Give the extent of all Babesia divergens-infected red blood cells.
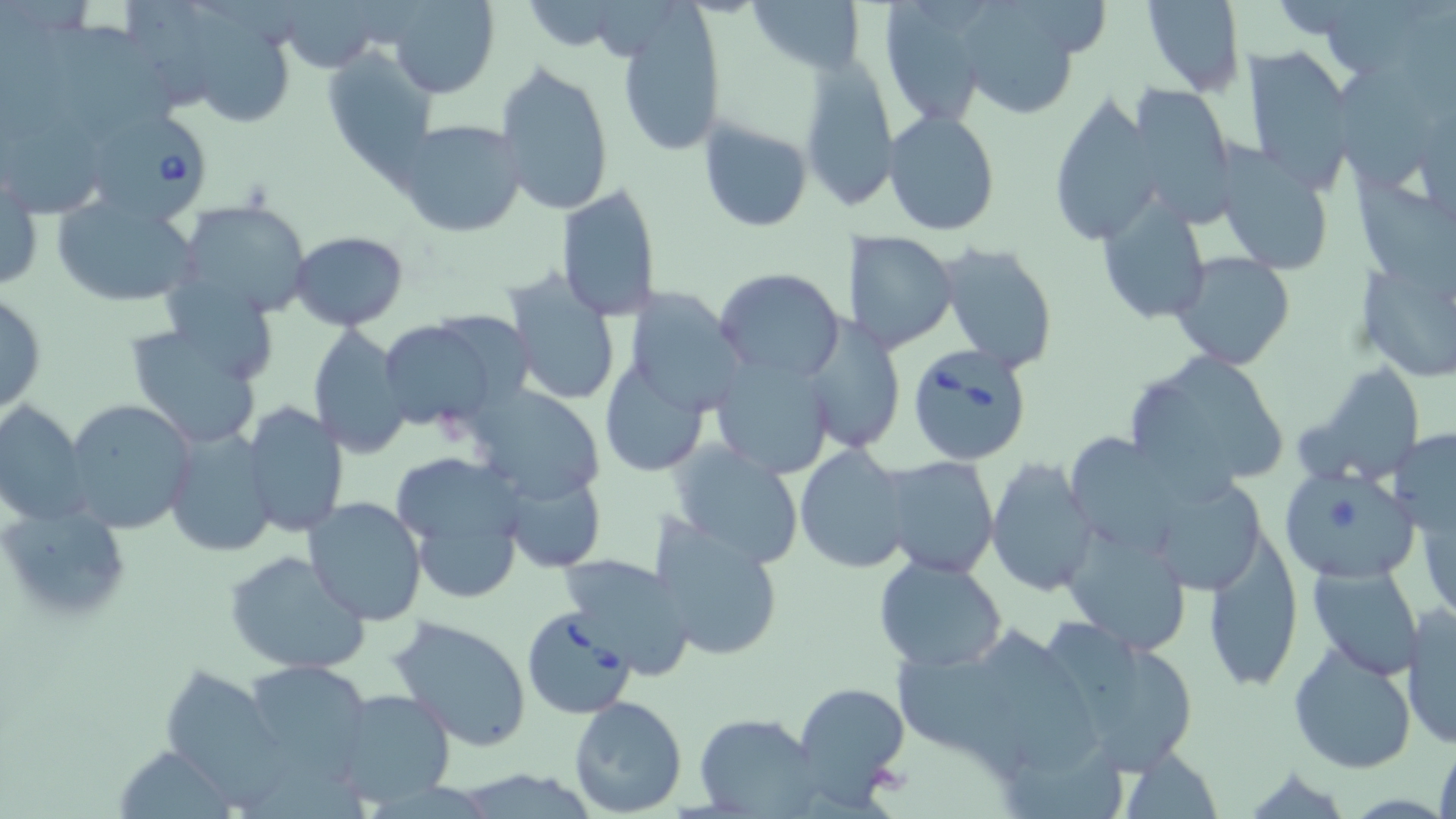
Approximate bounding boxes as (x1,y1)-(x2,y2) corner pairs in pixels.
Babesia divergens-infected red blood cells: (90,111)-(217,227), (905,342)-(1034,465), (521,607)-(637,721).

Uninfected red blood cell locations: (280,0)-(385,73), (387,0)-(500,99), (872,0)-(993,128), (1142,0)-(1244,95), (182,1)-(293,123), (747,1)-(867,74), (951,1)-(1092,122), (615,9)-(726,160), (47,18)-(178,137), (1238,45)-(1354,191), (322,49)-(438,175), (798,56)-(898,207), (495,59)-(616,218), (1336,65)-(1434,194), (1127,82)-(1238,223), (1046,93)-(1166,246), (882,110)-(1001,237), (396,118)-(527,237), (698,118)-(814,231), (0,119)-(114,217), (1214,147)-(1336,276), (1357,166)-(1456,292), (1,170)-(43,295), (554,182)-(661,321), (51,192)-(202,308), (176,197)-(312,317), (1098,200)-(1211,326), (848,230)-(959,353), (288,231)-(408,331), (935,242)-(1060,373), (1169,252)-(1296,371), (1358,259)-(1455,385), (503,267)-(626,408), (715,268)-(845,382), (620,289)-(746,418), (0,291)-(47,416), (377,315)-(516,435), (797,317)-(904,456), (123,319)-(266,449), (306,323)-(414,459), (1122,349)-(1290,497), (709,355)-(836,481), (1301,359)-(1428,487), (596,362)-(711,479), (465,384)-(607,505), (64,398)-(196,533), (0,400)-(90,528), (242,401)-(350,540), (164,427)-(277,557), (1390,429)-(1456,535), (1070,430)-(1184,560), (669,442)-(802,569), (793,444)-(916,573), (390,448)-(530,603), (877,454)-(1000,578), (986,457)-(1098,597), (1279,466)-(1420,584), (503,469)-(605,572), (303,497)-(428,624), (2,503)-(133,627), (1059,519)-(1194,657), (650,521)-(785,663), (1203,531)-(1304,693), (225,549)-(369,679), (557,552)-(696,683), (872,554)-(1009,674), (1303,560)-(1429,680), (1401,604)-(1455,749), (388,615)-(531,751), (1035,616)-(1203,778), (893,621)-(1102,778), (1287,641)-(1418,774), (250,661)-(366,782), (163,663)-(290,810), (793,682)-(910,804), (330,688)-(456,808), (569,696)-(687,818), (695,711)-(824,816), (1434,732)-(1456,819), (123,742)-(231,819), (1115,743)-(1224,817). Slide-level diagnosis: Babesia divergens. One field of a larger specimen. May-Grünwald-Giemsa stain. Light microscopy. 1000x magnification. Thin blood smear. Image is 1456×819 pixels.